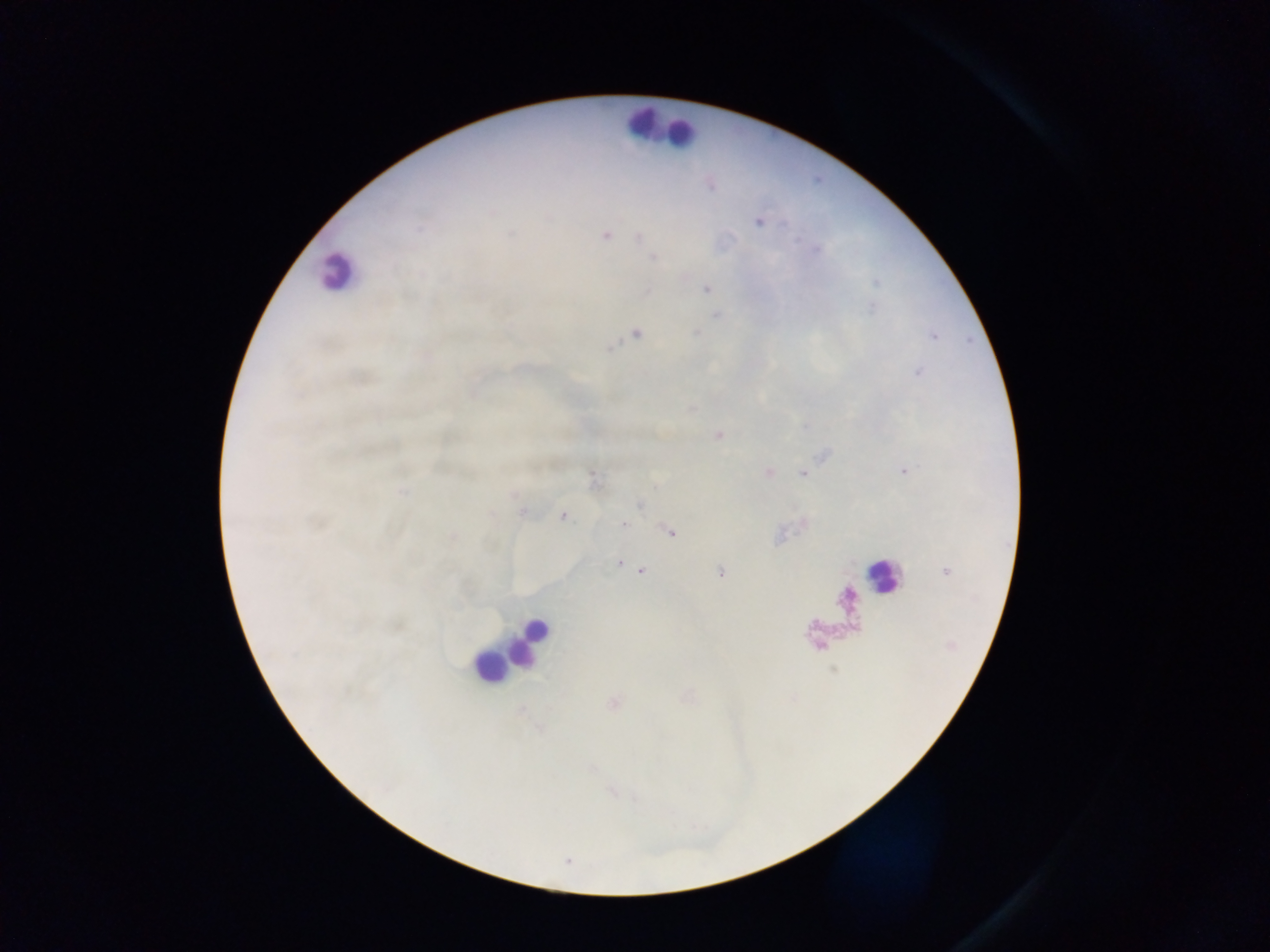
Approximate centers as (x, y) in pixels.
Summary:
  - Plasmodium parasite locations: (758, 222), (420, 229), (606, 236), (638, 237), (654, 258), (706, 288), (636, 334), (610, 348), (719, 435), (904, 471), (804, 473), (640, 505), (563, 516), (624, 524), (669, 532), (620, 564), (641, 571), (720, 573)
  - Leukocyte locations: (649, 124), (673, 129), (337, 272), (880, 575), (528, 641), (489, 666)
  - Capture: mobile-phone photograph through a microscope
  - Country: Ghana
  - Preparation: thick blood film
  - Image size: 1270×952 pixels
  - Field of view: single